Locate every Plasmodium parasite.
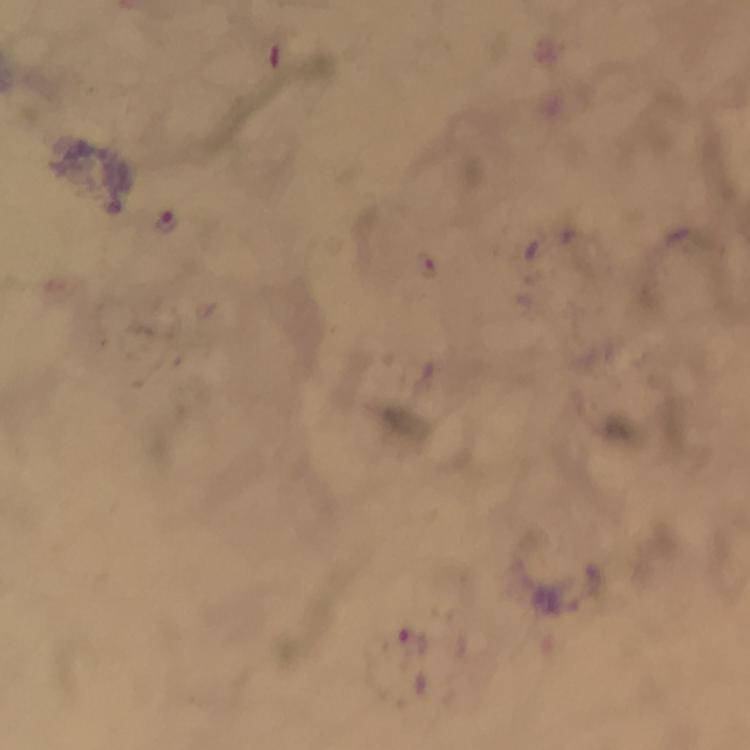
Approximate centers as [x, y] in pixels.
Plasmodium parasites: [166, 223], [412, 642].

From a malaria diagnostic workup. Immersion oil applied. Image is 750×750 pixels. Photographed with a smartphone mounted on the microscope. Giemsa-stained preparation. Thick smear. At 100x magnification. A crop from one field of view.